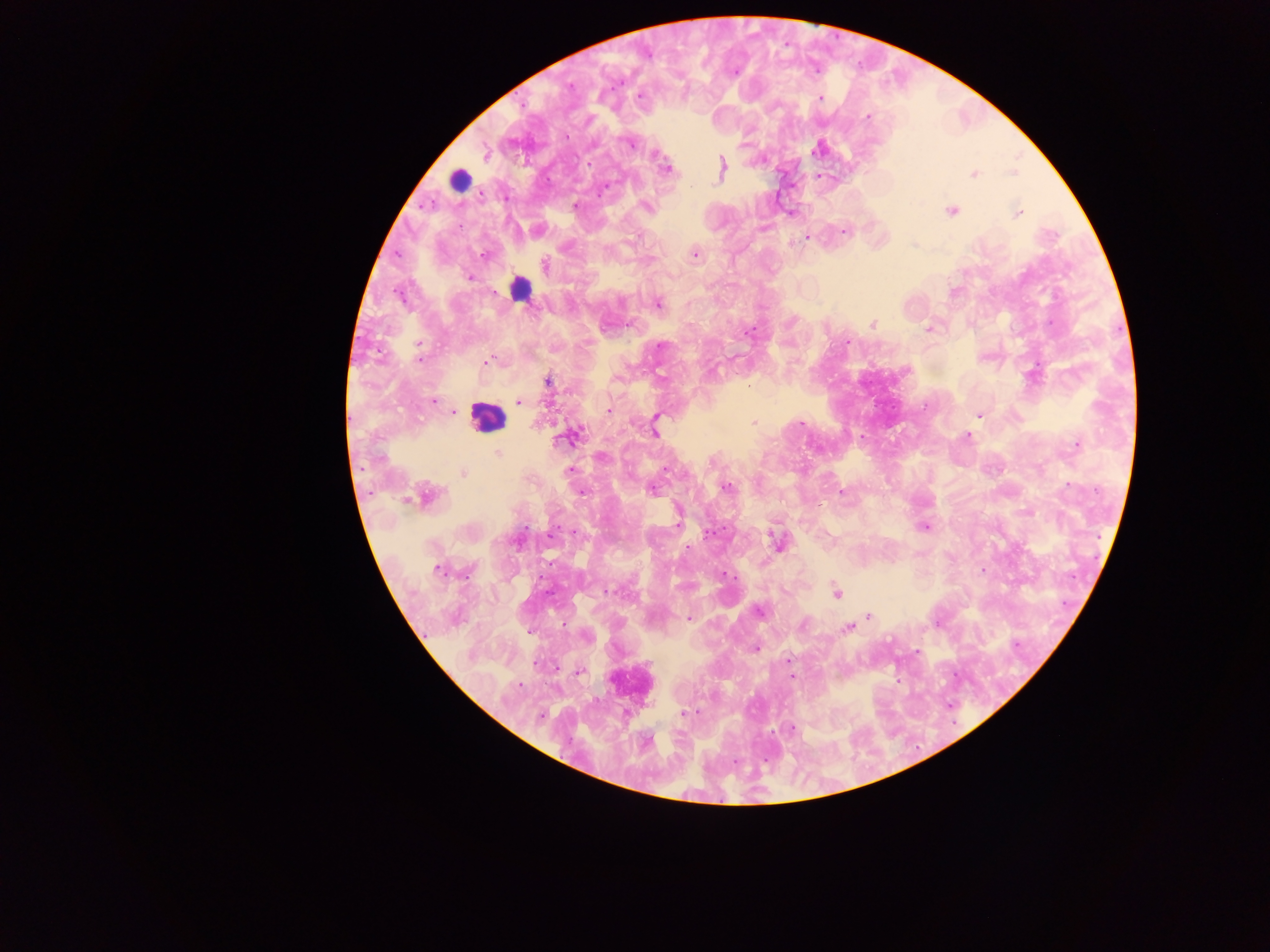

leukocyte locations = approximate centers as {x, y} in pixels: {459, 180}, {519, 289}, {488, 418}
image size = 1270×952 pixels
capture = mobile-phone photograph through a microscope
country = Ghana
malaria parasite locations = approximate centers as {x, y} in pixels: {735, 72}, {570, 86}, {639, 96}, {820, 98}, {867, 117}, {567, 137}, {630, 145}, {486, 155}, {589, 163}, {723, 164}, {665, 169}, {974, 174}, {818, 176}, {601, 193}, {575, 205}, {646, 207}, {951, 210}, {1017, 213}, {843, 231}, {807, 238}, {694, 254}, {484, 255}, {544, 264}, {469, 277}, {658, 304}, {872, 324}, {929, 329}, {749, 332}, {847, 342}, {418, 344}, {660, 346}, {420, 359}, {487, 362}, {548, 382}, {748, 385}, {434, 401}, {518, 402}, {608, 410}, {454, 412}, {979, 415}, {656, 417}, {754, 422}, {801, 422}, {655, 434}, {572, 436}, {967, 436}, {1076, 446}, {497, 452}, {667, 468}, {570, 469}, {463, 473}, {1068, 485}, {727, 487}, {653, 490}, {582, 492}, {842, 492}, {426, 495}, {677, 522}, {924, 527}, {573, 533}, {709, 534}, {778, 542}, {983, 570}, {438, 571}, {724, 573}, {610, 592}, {836, 593}, {759, 611}, {868, 617}, {689, 618}, {802, 625}, {848, 628}, {586, 636}, {756, 649}, {916, 652}, {536, 665}, {578, 671}, {792, 676}, {520, 685}, {683, 713}, {695, 713}, {540, 716}, {791, 728}
preparation = thick blood film
field of view = single